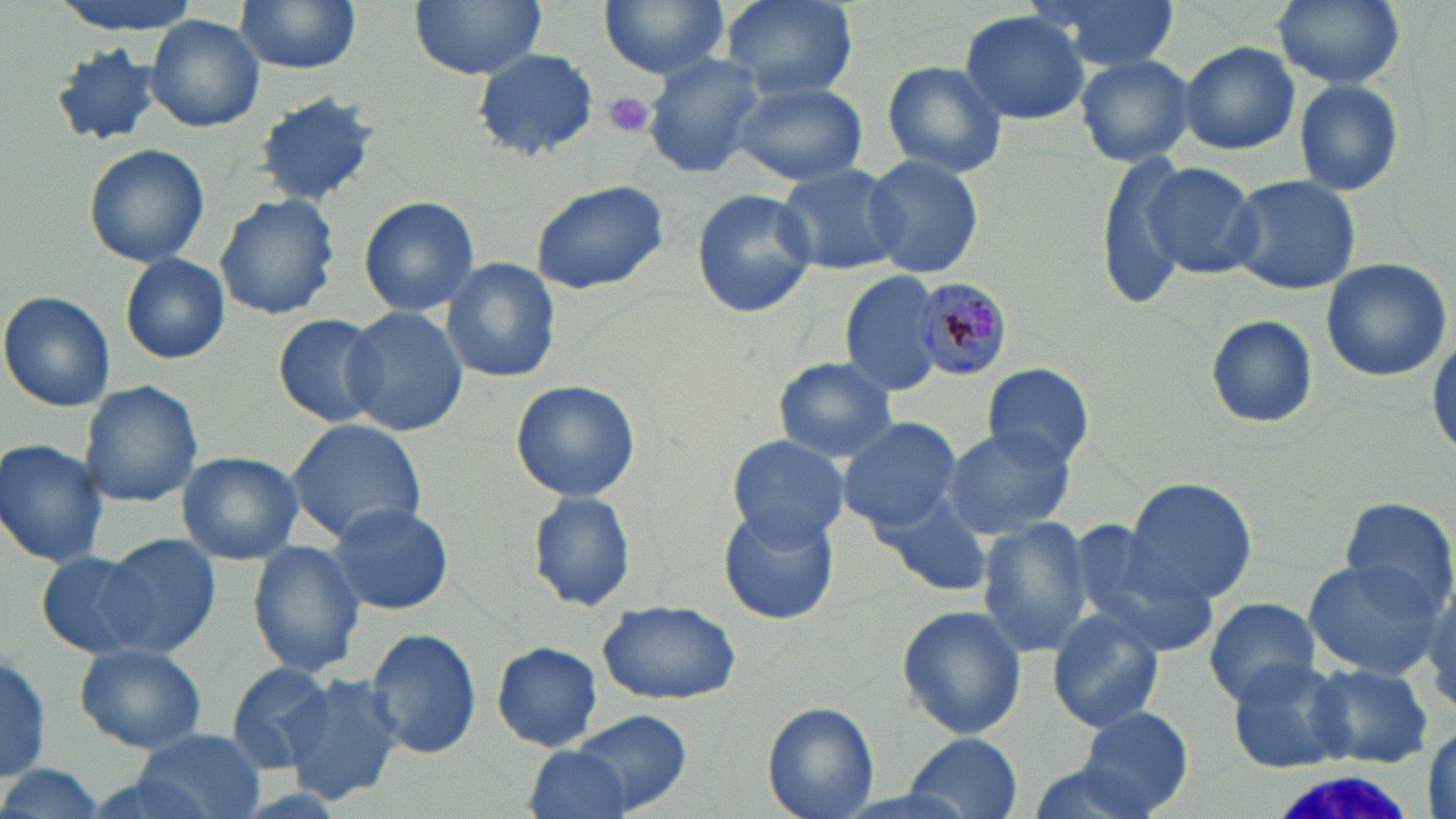

Summary:
  - Coordinate format: approximate bounding boxes as (x1, y1, x2, y2) in pixels
  - Uninfected red blood cell locations: (43, 0, 204, 35), (234, 0, 364, 74), (409, 0, 545, 79), (596, 0, 732, 79), (721, 0, 859, 99), (1034, 0, 1179, 70), (1273, 0, 1403, 89), (957, 10, 1092, 125), (145, 14, 265, 134), (1178, 41, 1301, 155), (48, 43, 161, 148), (472, 48, 596, 159), (642, 52, 769, 179), (1076, 54, 1194, 166), (881, 60, 1009, 178), (1292, 77, 1405, 199), (734, 82, 867, 185), (254, 93, 382, 207), (83, 142, 210, 268), (1093, 151, 1203, 308), (865, 153, 985, 281), (773, 162, 905, 276), (1142, 164, 1263, 278), (1227, 175, 1361, 295), (529, 179, 669, 296), (692, 188, 814, 320), (214, 194, 340, 321), (358, 194, 480, 317), (120, 253, 231, 365), (441, 257, 561, 384), (1320, 257, 1453, 383), (839, 270, 947, 396), (0, 290, 116, 412), (341, 307, 469, 437), (271, 313, 389, 429), (1205, 316, 1319, 431), (1430, 333, 1455, 462), (771, 357, 896, 462), (981, 363, 1095, 470), (509, 379, 641, 502), (77, 380, 203, 507), (837, 416, 958, 530), (286, 419, 428, 544), (941, 427, 1073, 540), (727, 435, 847, 546), (0, 439, 110, 569), (177, 451, 303, 565), (1125, 478, 1255, 603), (873, 487, 991, 597), (527, 489, 638, 612), (1337, 497, 1455, 610), (328, 501, 455, 616), (717, 503, 838, 625), (977, 518, 1095, 657), (1067, 519, 1221, 652), (101, 534, 221, 657), (247, 540, 367, 678), (35, 550, 157, 658), (1304, 557, 1447, 679), (1204, 596, 1322, 706), (596, 601, 740, 707), (896, 604, 1027, 741), (1045, 610, 1165, 733), (366, 628, 482, 760), (490, 642, 604, 752), (74, 643, 207, 754), (0, 650, 51, 784), (223, 658, 338, 770), (1225, 660, 1355, 774), (1307, 663, 1438, 768), (284, 672, 406, 805), (762, 701, 881, 819), (1075, 706, 1194, 816), (570, 709, 692, 815), (1425, 728, 1455, 813), (133, 729, 264, 818), (906, 733, 1025, 816), (521, 745, 637, 819), (0, 766, 106, 819)
  - Plasmodium malariae-infected red blood cell locations: (911, 275, 1017, 380)
  - White blood cell locations: (1262, 766, 1411, 819)
  - Platelet locations: (603, 91, 656, 137)
  - Slide-level diagnosis: Plasmodium malariae
  - Image size: 1456×819 pixels
  - Stain: May-Grünwald-Giemsa
  - Magnification: 1000x
  - Field of view: single
  - Preparation: thin blood smear
  - Modality: light microscopy